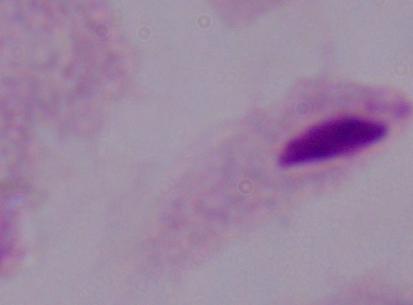

magnification = 1000x
identification = trichomonad
modality = photomicrograph